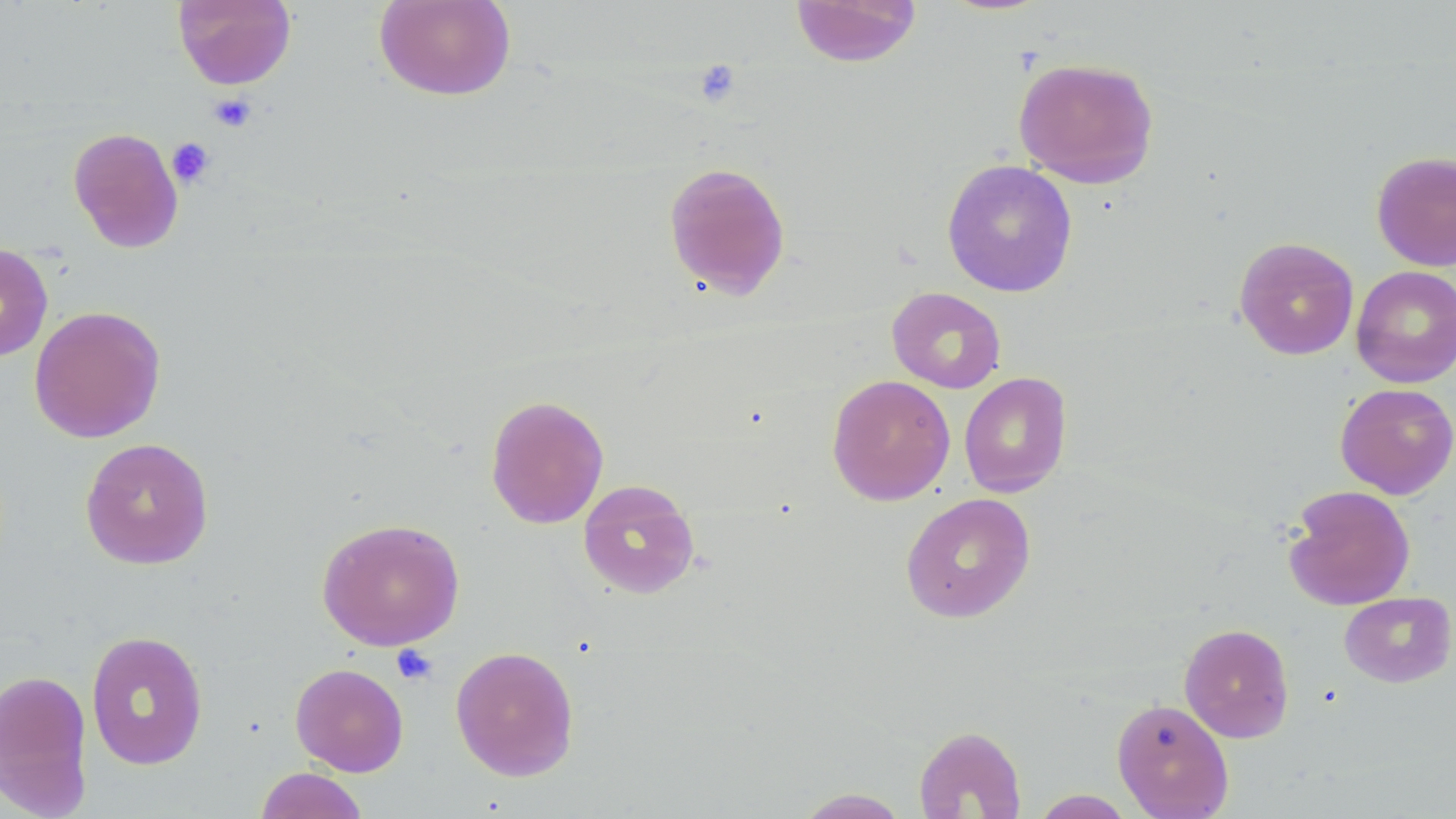 Approximate bounding boxes as [x1, y1, x2, y2] in pixels. Uninfected red blood cell locations: [173, 0, 297, 90], [374, 0, 517, 101], [790, 0, 922, 67], [1012, 57, 1160, 190], [67, 127, 184, 253], [1371, 151, 1456, 271], [941, 159, 1078, 298], [663, 161, 791, 301], [1234, 236, 1359, 360], [0, 242, 53, 362], [1351, 265, 1456, 388], [887, 287, 1006, 394], [29, 305, 166, 444], [958, 372, 1072, 498], [827, 374, 955, 506], [1335, 383, 1456, 499], [485, 394, 610, 529], [80, 437, 214, 569], [577, 479, 700, 600], [1283, 484, 1416, 611], [900, 492, 1036, 624], [316, 517, 465, 651], [1339, 591, 1455, 688], [1179, 623, 1295, 743], [85, 630, 209, 770], [450, 645, 580, 781], [290, 662, 409, 776], [0, 668, 93, 816], [1111, 698, 1234, 818], [912, 725, 1027, 818], [254, 767, 368, 819], [793, 787, 911, 818], [1030, 790, 1137, 818]. Platelet locations: [693, 60, 742, 107], [208, 94, 257, 133], [166, 137, 215, 188], [391, 644, 438, 686]. Slide-level diagnosis: negative for blood parasites. May-Grünwald-Giemsa stain. One field of a larger specimen. 1000x magnification. Image is 1456×819 pixels. Light microscopy. Thin blood smear.